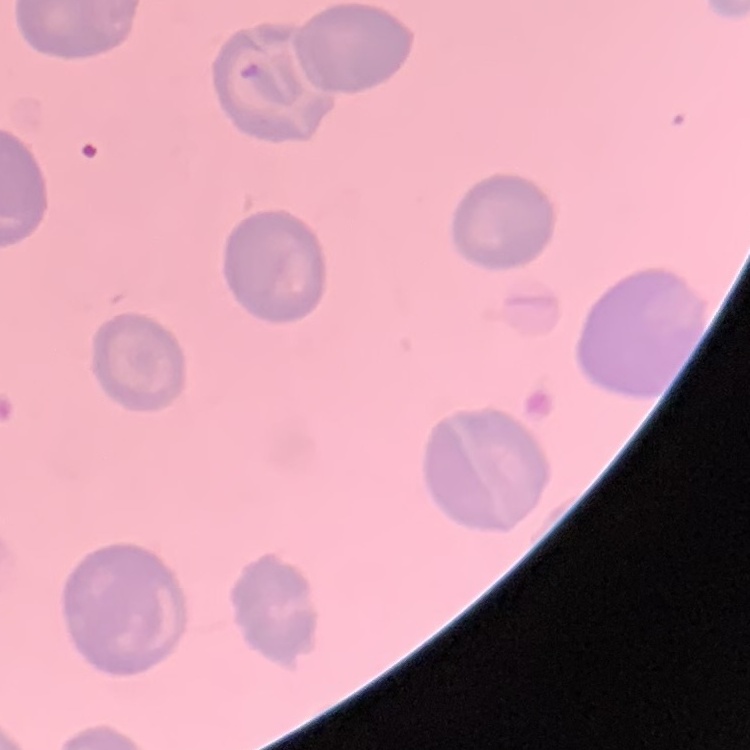 The red blood cells show no rouleaux formation. One tile cut from a larger photomicrograph. Stained with either Field's or Giemsa. Thin blood film.